Identify the blood parasite species.
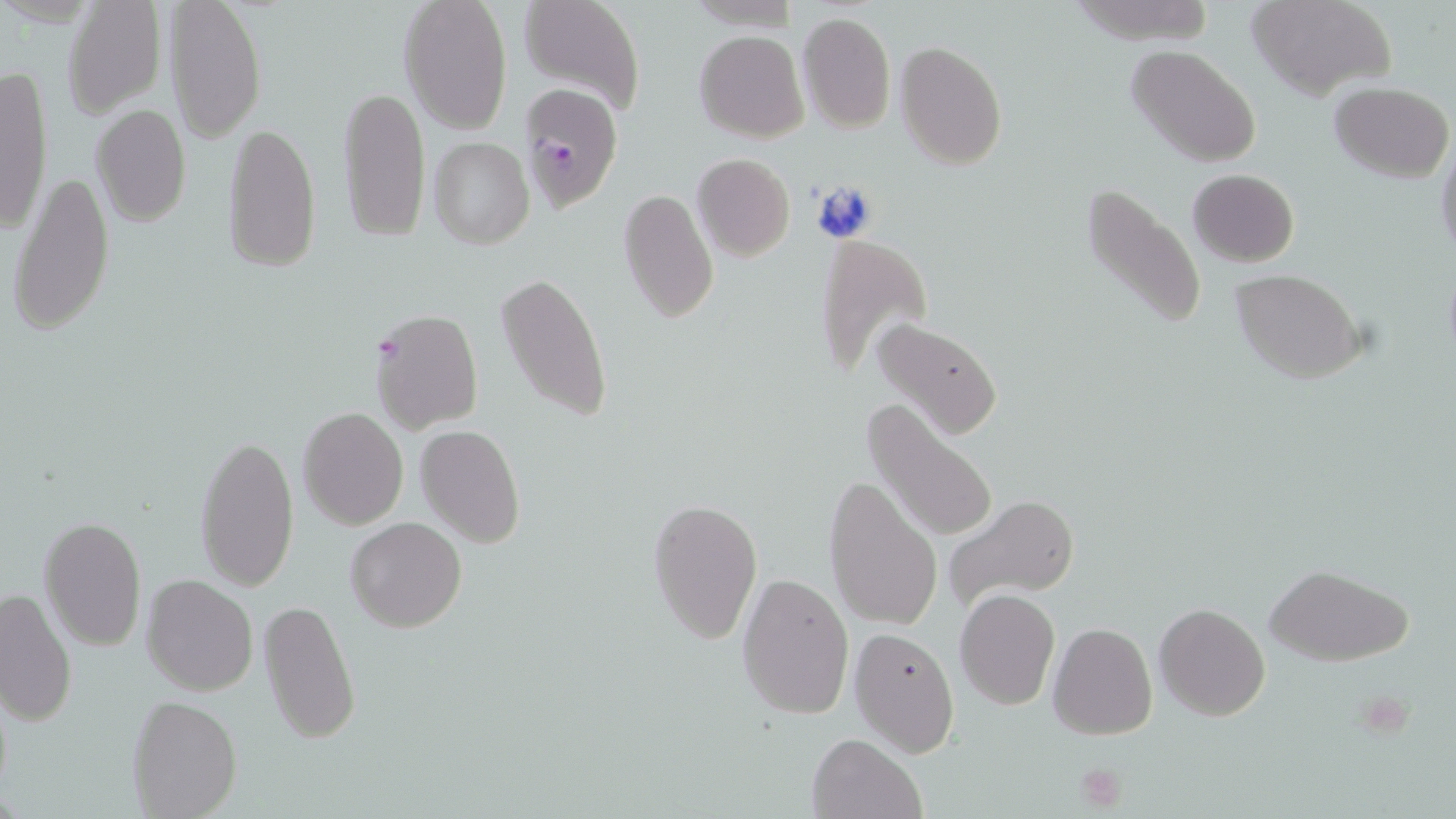
Plasmodium falciparum.

magnification = 1000x
Plasmodium falciparum-infected red blood cell locations = approximate bounding boxes as [x1, y1, x2, y2] in pixels: [518, 82, 624, 211], [369, 307, 485, 434]
modality = optical microscopy
platelet locations = approximate bounding boxes as [x1, y1, x2, y2] in pixels: [1070, 761, 1131, 811]
preparation = thin blood film
field of view = one of a larger specimen
stain = May-Grünwald-Giemsa
uninfected red blood cell locations = approximate bounding boxes as [x1, y1, x2, y2] in pixels: [167, 0, 267, 143], [399, 0, 513, 134], [516, 0, 646, 117], [1248, 0, 1397, 101], [61, 1, 168, 119], [798, 9, 896, 134], [695, 30, 808, 142], [896, 41, 1008, 170], [1126, 46, 1261, 167], [0, 60, 54, 236], [339, 81, 430, 243], [1330, 82, 1453, 181], [90, 104, 192, 227], [222, 118, 321, 274], [427, 137, 534, 250], [1435, 140, 1456, 267], [692, 154, 795, 261], [9, 169, 114, 339], [1188, 169, 1299, 266], [1080, 179, 1208, 334], [618, 187, 719, 324], [814, 233, 932, 384], [495, 269, 614, 424], [1231, 270, 1366, 383], [870, 318, 1005, 441], [866, 398, 999, 548], [297, 408, 409, 530], [416, 424, 525, 549], [193, 432, 299, 594], [824, 473, 942, 632], [943, 491, 1080, 614], [646, 496, 762, 647], [39, 516, 149, 653], [345, 517, 467, 634], [1262, 562, 1414, 665], [736, 571, 854, 719], [142, 572, 259, 696], [0, 586, 77, 726], [955, 589, 1060, 711], [259, 597, 359, 745], [1154, 602, 1271, 720], [1048, 622, 1158, 738], [848, 626, 960, 757], [127, 695, 242, 817], [805, 732, 925, 819]
image size = 1456×819 pixels